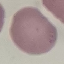

Summary:
  - Malaria status: uninfected
  - Stain: Giemsa
  - Image type: automatically extracted cell patch, resized to 64 × 64 pixels
  - Preparation: thin blood smear
  - Capture: smartphone camera at the microscope eyepiece